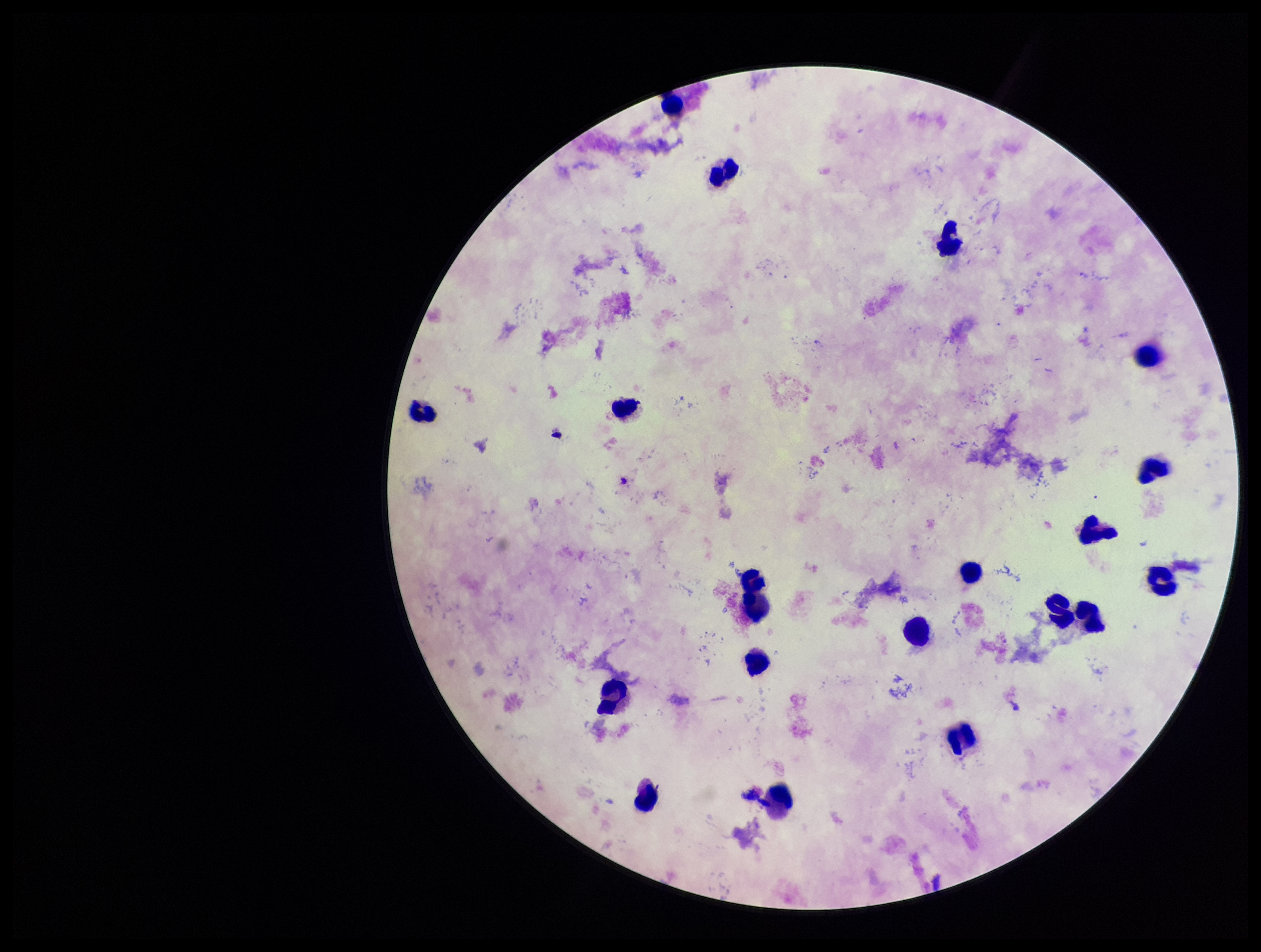
Single field of view. Species reported for this patient: Plasmodium falciparum. Patient malaria status: infected. Photographed through the microscope eyepiece with a smartphone camera. Plasmodium parasites: none seen. Parasite count: 0. Giemsa stain. Image is 1261×952 pixels. Leukocyte count: 19. Preparation: thick blood smear.